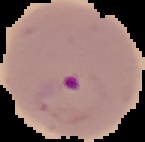

The area outside the segmented cell region is set to black. Result: Plasmodium parasites detected. From a thin blood film. Image is 145×142 pixels.